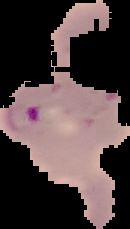
Summary:
  - Image type: cell region segmented out of the field of view; surrounding area masked to black
  - Result: Plasmodium parasites detected
  - Preparation: thin blood film
  - Image size: 130×229 pixels